Report the malaria status of this cell.
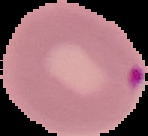

It is parasitized.

{
  "image_size": "148×136 pixels",
  "image_type": "segmented cell region with the area outside set to black",
  "preparation": "thin blood film"
}